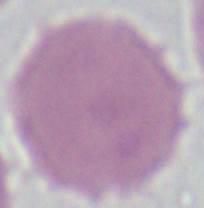

{
  "identification": "red blood cell",
  "modality": "micrograph",
  "magnification": "1000x"
}